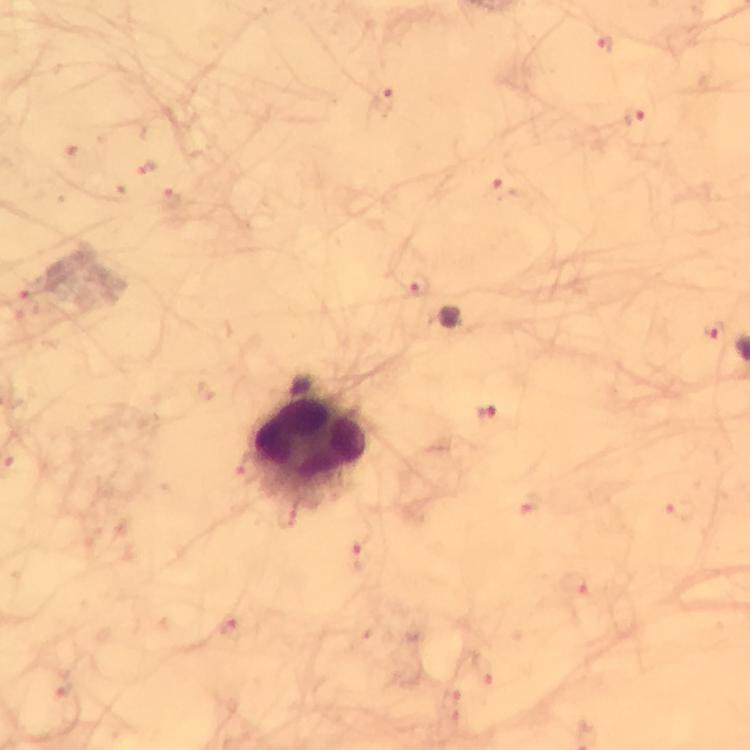

Approximate centers as (x, y) in pixels. Leukocyte locations: (308, 443). Malaria parasite locations: (604, 45), (637, 116), (503, 189), (413, 283), (713, 328), (487, 414). Immersion oil applied. 100x magnification. A crop from one field of view. From a diagnostic examination for malaria. Image is 750×750 pixels. Smartphone photograph taken through a microscope. Giemsa-stained preparation. Thick blood smear.